Assess this cell for malaria.
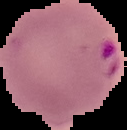
Parasitized.

From a thin blood film. Image is 127×130 pixels. Segmented cell region on a black background.